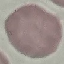
malaria status = uninfected
capture = smartphone through the microscope eyepiece
image type = automatically extracted cell patch, resized to 64 × 64 pixels
stain = Giemsa
preparation = thin blood film